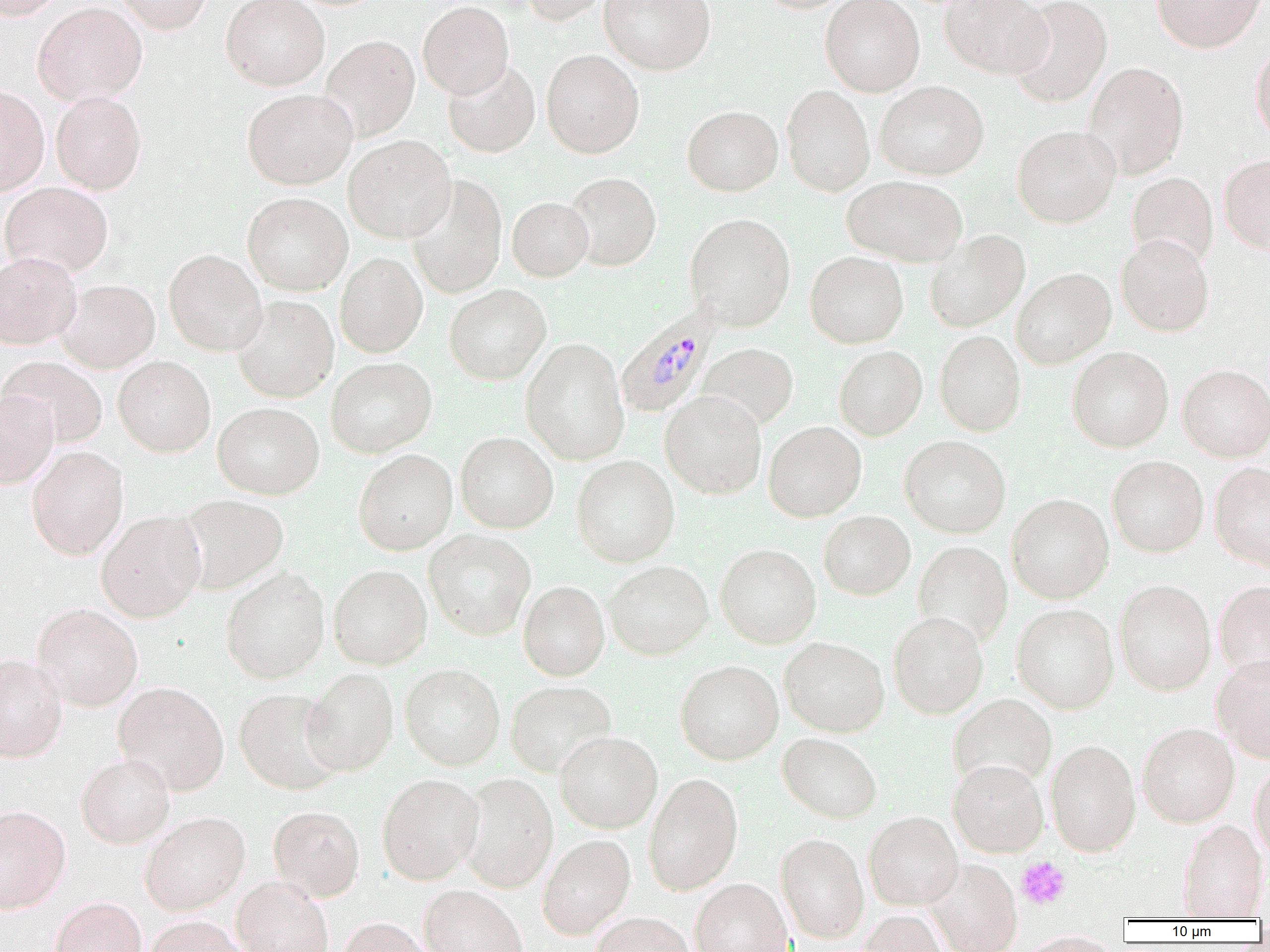

Approximate bounding boxes as (x1,y1)-(x2,y2) corner pairs in pixels. Plasmodium malariae-infected red blood cell locations: (615,306)-(720,419). Uninfected red blood cell locations: (0,0)-(67,20), (114,0)-(213,34), (220,0)-(330,90), (516,0)-(611,25), (598,0)-(715,75), (755,0)-(856,13), (820,0)-(925,97), (940,0)-(1053,79), (1009,0)-(1112,109), (1151,0)-(1267,53), (417,1)-(514,99), (32,2)-(147,106), (320,35)-(420,141), (1250,41)-(1270,147), (542,49)-(644,158), (442,59)-(540,158), (1083,62)-(1189,179), (875,80)-(989,180), (781,84)-(875,196), (0,85)-(50,195), (242,88)-(357,189), (51,91)-(147,194), (682,105)-(783,196), (1012,125)-(1120,228), (343,135)-(456,243), (1218,153)-(1270,254), (1127,171)-(1219,268), (564,172)-(661,271), (842,174)-(967,267), (406,175)-(507,299), (1,181)-(113,278), (242,192)-(353,296), (507,197)-(593,281), (685,213)-(796,330), (925,230)-(1030,332), (1116,234)-(1215,336), (164,249)-(267,356), (805,251)-(908,349), (0,252)-(82,350), (335,252)-(428,357), (1011,268)-(1116,368), (58,279)-(159,373), (444,284)-(551,384), (231,296)-(339,402), (935,330)-(1026,436), (520,338)-(629,465), (698,342)-(799,430), (834,345)-(927,440), (1067,346)-(1173,452), (1,356)-(107,448), (113,356)-(215,457), (326,356)-(436,457), (1177,364)-(1270,461), (0,391)-(58,489), (660,391)-(767,498), (213,401)-(324,499), (763,421)-(866,522), (455,431)-(559,534), (899,435)-(1010,538), (26,445)-(129,560), (353,449)-(457,555), (571,454)-(679,567), (1107,455)-(1208,557), (1210,462)-(1270,572), (1006,493)-(1113,603), (175,494)-(288,595), (96,510)-(206,622), (818,510)-(915,600), (423,529)-(536,640), (913,540)-(1012,646), (715,543)-(821,648), (604,560)-(713,659), (329,563)-(432,669), (318,565)-(412,776), (221,568)-(330,683), (1114,579)-(1216,696), (1213,579)-(1270,684), (518,580)-(610,680), (31,603)-(143,711), (1012,603)-(1119,713), (887,611)-(989,719), (779,636)-(889,737), (0,654)-(67,762), (1212,654)-(1270,761), (675,659)-(784,765), (400,663)-(505,770), (302,667)-(399,776), (505,680)-(616,777), (113,681)-(229,795), (234,688)-(343,794), (948,693)-(1057,789), (1137,722)-(1240,827), (554,730)-(663,833), (777,732)-(882,823), (1045,739)-(1141,856), (75,754)-(175,848), (947,758)-(1048,858), (1249,761)-(1270,863), (458,772)-(558,892), (643,772)-(743,895), (377,773)-(484,884), (0,805)-(71,913), (268,805)-(365,901), (863,810)-(963,909), (139,811)-(250,915), (1177,818)-(1267,919), (775,832)-(869,943), (537,834)-(636,939), (924,860)-(1022,951), (231,876)-(333,952), (690,878)-(793,952), (418,884)-(527,952), (49,896)-(147,952), (856,910)-(951,952), (590,913)-(695,951), (144,915)-(250,952), (336,917)-(435,952), (1012,931)-(1122,952). Platelet locations: (1017,857)-(1070,909). Slide-level diagnosis: Plasmodium malariae. 1000x magnification. Thin blood smear. Image is 1270×952 pixels. Light microscopy. One field of a larger specimen.